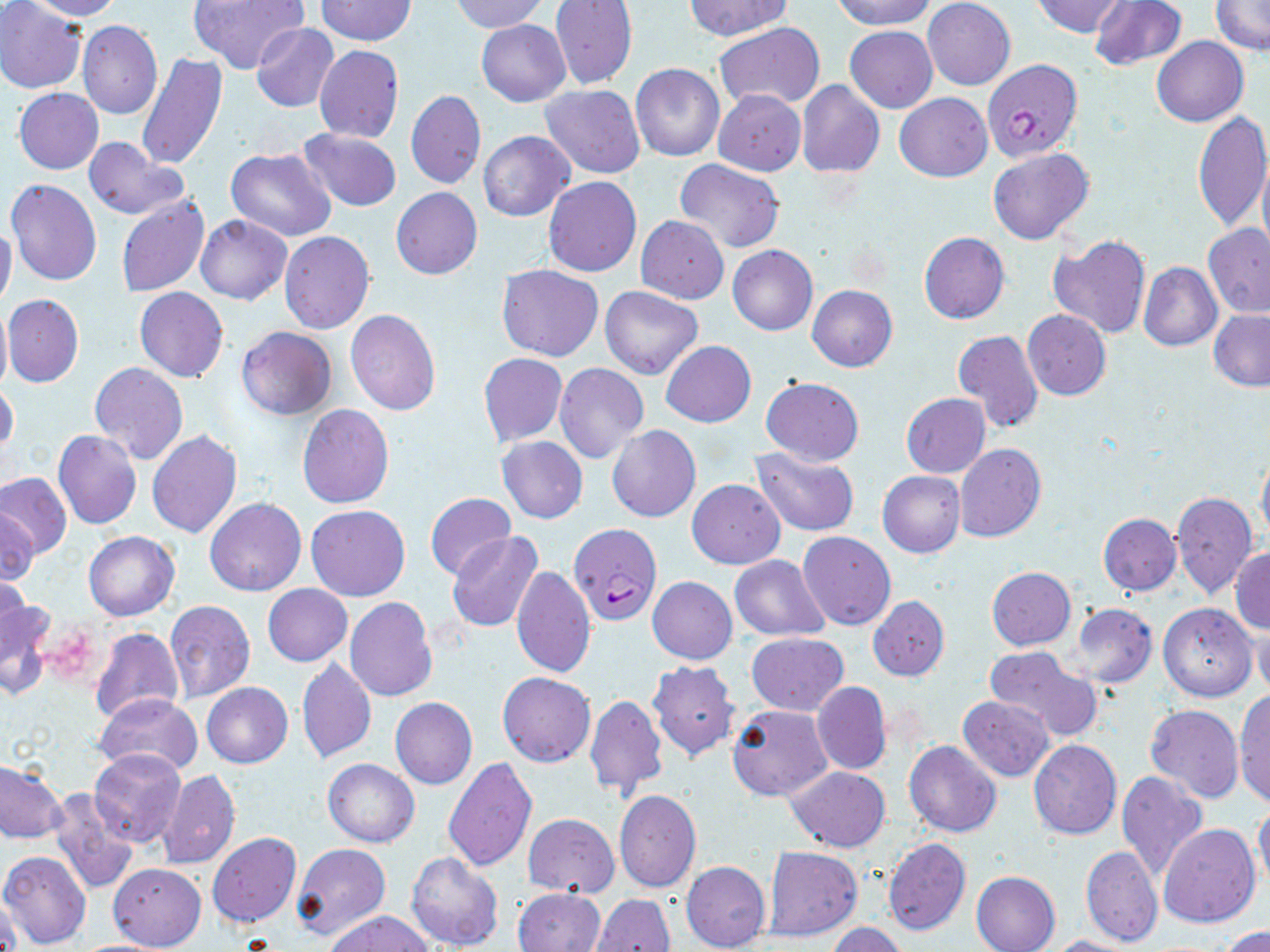

slide-level diagnosis = Plasmodium falciparum
field of view = single
image size = 1270×952 pixels
Plasmodium falciparum-infected red blood cell locations = approximate bounding boxes as [x1, y1, x2, y2] in pixels: [983, 59, 1081, 161], [569, 524, 660, 624]
preparation = thin blood smear
stain = May-Grünwald-Giemsa
uninfected red blood cell locations = approximate bounding boxes as [x1, y1, x2, y2] in pixels: [0, 0, 86, 94], [21, 0, 124, 21], [187, 0, 308, 74], [685, 0, 792, 40], [833, 0, 934, 30], [923, 0, 1015, 90], [1032, 0, 1127, 37], [1088, 0, 1188, 71], [1211, 0, 1269, 53], [315, 1, 416, 46], [449, 1, 547, 34], [549, 1, 637, 90], [77, 19, 164, 120], [476, 19, 570, 106], [714, 22, 826, 111], [250, 23, 339, 113], [845, 26, 937, 113], [1153, 37, 1248, 126], [313, 45, 404, 143], [136, 54, 228, 169], [630, 63, 725, 162], [797, 80, 884, 178], [540, 84, 644, 179], [14, 88, 104, 174], [713, 89, 805, 176], [406, 90, 486, 189], [895, 92, 992, 181], [1191, 111, 1270, 232], [296, 129, 403, 212], [479, 131, 573, 221], [83, 136, 188, 219], [225, 147, 336, 241], [987, 148, 1094, 245], [1257, 150, 1270, 263], [675, 157, 785, 253], [5, 177, 102, 286], [544, 177, 640, 276], [391, 187, 482, 279], [116, 195, 209, 297], [195, 214, 291, 304], [636, 215, 729, 304], [0, 221, 17, 315], [1203, 223, 1270, 318], [279, 231, 374, 333], [919, 233, 1009, 324], [1049, 235, 1151, 338], [727, 244, 818, 336], [1138, 262, 1222, 350], [496, 264, 603, 360], [600, 286, 703, 379], [807, 286, 898, 372], [134, 287, 228, 383], [3, 293, 83, 387], [0, 304, 11, 394], [345, 310, 441, 414], [1022, 310, 1112, 399], [1208, 310, 1270, 391], [237, 327, 336, 421], [952, 329, 1043, 432], [660, 341, 756, 427], [479, 352, 567, 446], [89, 362, 188, 465], [555, 363, 648, 462], [760, 377, 864, 466], [0, 382, 19, 460], [900, 393, 991, 477], [297, 404, 394, 508], [608, 425, 701, 522], [53, 429, 142, 529], [147, 430, 242, 539], [497, 436, 588, 523], [955, 443, 1046, 542], [751, 445, 859, 536], [1256, 445, 1270, 542], [878, 470, 965, 557], [0, 471, 71, 560], [687, 479, 785, 569], [1171, 491, 1258, 599], [425, 494, 516, 580], [205, 498, 306, 597], [306, 505, 410, 601], [1, 507, 38, 589], [1098, 513, 1180, 595], [83, 531, 179, 621], [798, 531, 895, 630], [447, 533, 543, 633], [1230, 548, 1270, 635], [728, 555, 830, 641], [511, 566, 595, 679], [987, 566, 1076, 650], [1, 567, 29, 657], [648, 576, 738, 664], [262, 584, 352, 666], [0, 593, 55, 700], [869, 596, 949, 681], [345, 597, 437, 700], [165, 600, 255, 704], [1158, 603, 1257, 702], [1070, 604, 1157, 688], [1253, 617, 1270, 700], [90, 628, 182, 726], [746, 632, 849, 716], [984, 646, 1102, 742], [296, 658, 376, 764], [648, 660, 739, 759], [497, 673, 595, 766], [201, 682, 293, 769], [812, 682, 891, 775], [1233, 689, 1270, 807], [95, 692, 202, 777], [583, 692, 668, 799], [958, 694, 1054, 781], [389, 697, 477, 790], [727, 703, 834, 801], [1144, 705, 1245, 804], [1028, 740, 1121, 839], [905, 741, 1001, 837], [89, 749, 186, 848], [441, 756, 537, 873], [323, 758, 419, 847], [0, 761, 67, 843], [786, 766, 890, 853], [158, 770, 240, 870], [1116, 770, 1207, 881], [1089, 788, 1185, 932], [47, 789, 139, 893], [614, 790, 701, 894], [1253, 803, 1270, 891], [522, 813, 619, 896], [1160, 823, 1261, 928], [208, 832, 302, 927], [883, 838, 971, 936], [292, 844, 392, 942], [763, 846, 862, 941], [1080, 847, 1163, 947], [0, 850, 91, 950], [406, 851, 504, 950], [682, 860, 771, 952], [108, 863, 206, 949], [972, 871, 1061, 952], [515, 888, 605, 951], [591, 893, 674, 952], [1, 895, 20, 952], [325, 910, 434, 952], [826, 922, 909, 952], [1219, 926, 1270, 952], [1043, 935, 1138, 952]
magnification = 1000x
modality = light microscopy